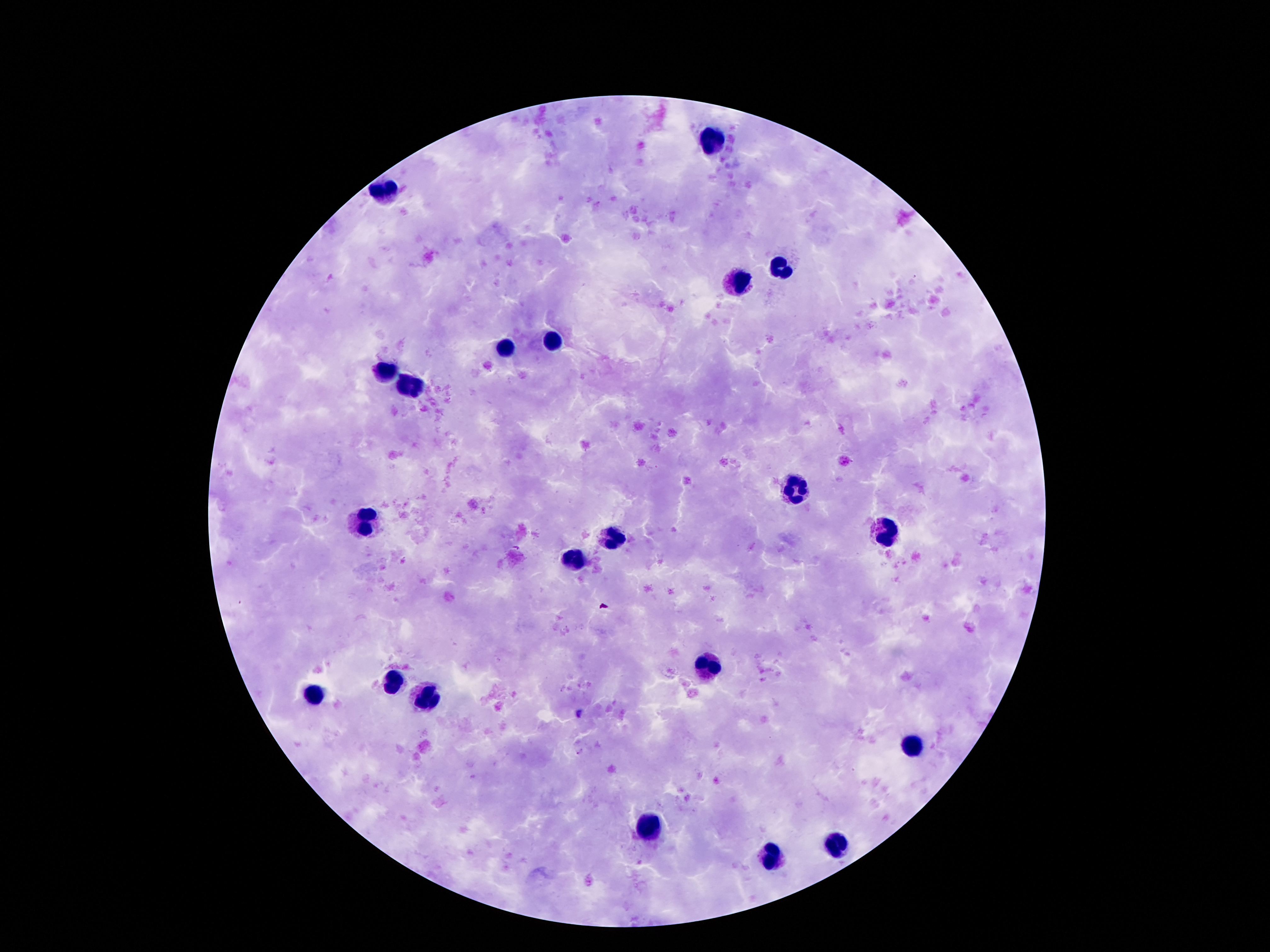
{
  "capture": "smartphone camera through the microscope eyepiece",
  "preparation": "thick peripheral-blood smear",
  "magnification": "100x",
  "patient_malaria_status": "not infected",
  "field_of_view": "one from this slide",
  "image_size": "1270×952 pixels",
  "leukocyte_locations": "approximate centers as {x, y} in pixels: {713, 138}, {387, 191}, {778, 267}, {734, 281}, {553, 342}, {509, 348}, {387, 375}, {410, 388}, {794, 489}, {366, 519}, {887, 532}, {612, 538}, {576, 561}, {713, 666}, {391, 681}, {311, 694}, {427, 696}, {912, 747}, {649, 824}, {838, 845}, {769, 855}",
  "stain": "Giemsa"
}